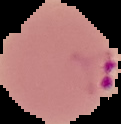
{
  "malaria_status": "parasitized",
  "image_type": "segmented cell region with the area outside set to black",
  "preparation": "thin blood film",
  "image_size": "121×124 pixels"
}